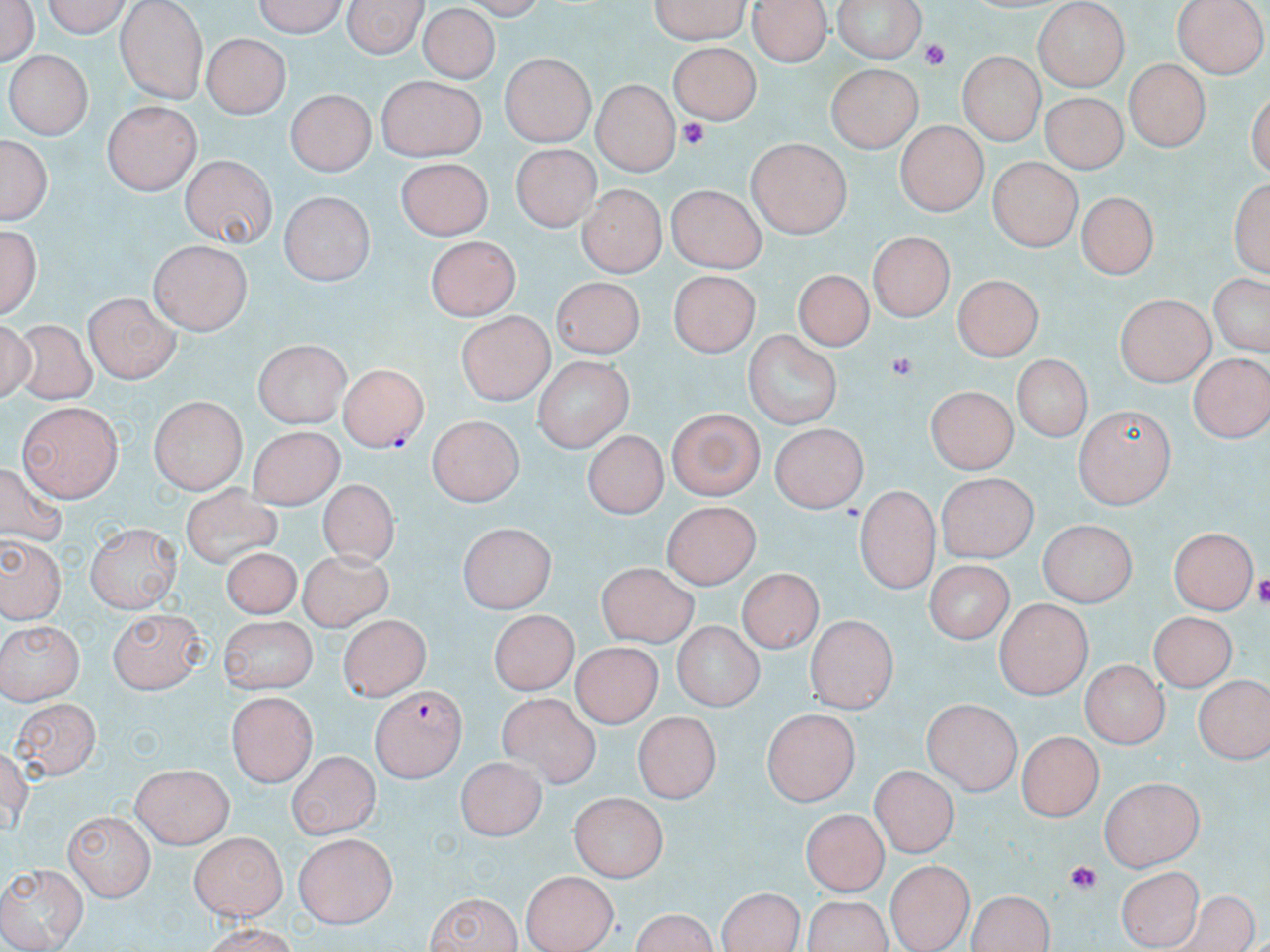

slide_level_diagnosis: Plasmodium falciparum
magnification: 1000x
image_size: 1270×952 pixels
modality: light microscopy
stain: May-Grünwald-Giemsa
field_of_view: one of a larger specimen
preparation: thin blood smear
platelet_locations: 'approximate bounding boxes as named x1/y1/x2/y2 corners in pixels: (x1=921, y1=40, x2=955, y2=70), (x1=676, y1=118, x2=709, y2=149), (x1=889, y1=353, x2=913, y2=379), (x1=1257, y1=575, x2=1270, y2=607), (x1=1065, y1=858, x2=1099, y2=896)'
plasmodium_falciparum_infected_red_blood_cell_locations: 'approximate bounding boxes as named x1/y1/x2/y2 corners in pixels: (x1=335, y1=364, x2=428, y2=452), (x1=370, y1=686, x2=465, y2=782)'
uninfected_red_blood_cell_locations: 'approximate bounding boxes as named x1/y1/x2/y2 corners in pixels: (x1=0, y1=0, x2=39, y2=70), (x1=35, y1=0, x2=134, y2=35), (x1=247, y1=0, x2=349, y2=35), (x1=345, y1=0, x2=421, y2=60), (x1=647, y1=0, x2=752, y2=39), (x1=831, y1=0, x2=928, y2=61), (x1=1173, y1=0, x2=1266, y2=77), (x1=114, y1=1, x2=210, y2=103), (x1=749, y1=1, x2=833, y2=63), (x1=1032, y1=3, x2=1132, y2=89), (x1=421, y1=7, x2=497, y2=80), (x1=401, y1=21, x2=497, y2=133), (x1=203, y1=32, x2=287, y2=119), (x1=668, y1=40, x2=762, y2=127), (x1=959, y1=51, x2=1043, y2=143), (x1=10, y1=52, x2=92, y2=138), (x1=501, y1=55, x2=594, y2=147), (x1=1124, y1=59, x2=1208, y2=153), (x1=829, y1=66, x2=921, y2=152), (x1=374, y1=73, x2=488, y2=161), (x1=593, y1=79, x2=680, y2=173), (x1=286, y1=89, x2=373, y2=177), (x1=1041, y1=95, x2=1122, y2=174), (x1=101, y1=99, x2=199, y2=192), (x1=897, y1=121, x2=984, y2=218), (x1=0, y1=135, x2=54, y2=224), (x1=744, y1=137, x2=852, y2=239), (x1=510, y1=144, x2=600, y2=232), (x1=180, y1=155, x2=276, y2=249), (x1=989, y1=155, x2=1085, y2=248), (x1=394, y1=158, x2=492, y2=236), (x1=1231, y1=178, x2=1269, y2=276), (x1=667, y1=183, x2=766, y2=274), (x1=577, y1=185, x2=662, y2=277), (x1=1077, y1=191, x2=1157, y2=282), (x1=276, y1=192, x2=376, y2=285), (x1=1, y1=226, x2=43, y2=323), (x1=870, y1=231, x2=957, y2=318), (x1=427, y1=234, x2=523, y2=317), (x1=149, y1=240, x2=253, y2=335), (x1=669, y1=269, x2=761, y2=357), (x1=793, y1=269, x2=870, y2=353), (x1=1205, y1=271, x2=1268, y2=357), (x1=955, y1=273, x2=1045, y2=358), (x1=551, y1=277, x2=643, y2=355), (x1=81, y1=293, x2=182, y2=382), (x1=1115, y1=293, x2=1213, y2=385), (x1=456, y1=313, x2=553, y2=406), (x1=8, y1=324, x2=100, y2=403), (x1=741, y1=329, x2=845, y2=430), (x1=256, y1=341, x2=350, y2=428), (x1=1189, y1=351, x2=1270, y2=439), (x1=1009, y1=355, x2=1095, y2=441), (x1=533, y1=356, x2=632, y2=453), (x1=926, y1=388, x2=1021, y2=472), (x1=149, y1=396, x2=245, y2=492), (x1=17, y1=401, x2=119, y2=501), (x1=665, y1=407, x2=764, y2=499), (x1=1076, y1=407, x2=1175, y2=510), (x1=425, y1=416, x2=526, y2=504), (x1=768, y1=420, x2=867, y2=513), (x1=246, y1=425, x2=340, y2=510), (x1=581, y1=432, x2=668, y2=517), (x1=935, y1=474, x2=1034, y2=562), (x1=316, y1=481, x2=401, y2=565), (x1=177, y1=483, x2=284, y2=571), (x1=854, y1=487, x2=942, y2=591), (x1=664, y1=501, x2=761, y2=589), (x1=1037, y1=521, x2=1134, y2=607), (x1=86, y1=524, x2=181, y2=614), (x1=456, y1=524, x2=558, y2=613), (x1=1171, y1=525, x2=1258, y2=615), (x1=3, y1=537, x2=60, y2=622), (x1=221, y1=545, x2=299, y2=621), (x1=296, y1=552, x2=396, y2=631), (x1=928, y1=561, x2=1011, y2=641), (x1=598, y1=563, x2=698, y2=647), (x1=740, y1=567, x2=820, y2=654), (x1=994, y1=599, x2=1092, y2=696), (x1=105, y1=606, x2=206, y2=693), (x1=485, y1=608, x2=582, y2=692), (x1=1150, y1=609, x2=1239, y2=693), (x1=805, y1=614, x2=898, y2=714), (x1=336, y1=615, x2=429, y2=699), (x1=217, y1=617, x2=320, y2=695), (x1=0, y1=619, x2=84, y2=703), (x1=669, y1=625, x2=763, y2=709), (x1=571, y1=644, x2=661, y2=730), (x1=1083, y1=660, x2=1168, y2=747), (x1=1193, y1=675, x2=1267, y2=761), (x1=227, y1=690, x2=314, y2=787), (x1=497, y1=692, x2=600, y2=789), (x1=12, y1=697, x2=96, y2=778), (x1=920, y1=699, x2=1024, y2=793), (x1=762, y1=706, x2=864, y2=805), (x1=634, y1=711, x2=718, y2=805), (x1=1019, y1=729, x2=1101, y2=821), (x1=1, y1=745, x2=38, y2=837), (x1=289, y1=750, x2=379, y2=838), (x1=454, y1=756, x2=542, y2=840), (x1=131, y1=763, x2=231, y2=847), (x1=868, y1=766, x2=956, y2=856), (x1=1099, y1=776, x2=1206, y2=871), (x1=78, y1=787, x2=223, y2=865), (x1=573, y1=795, x2=667, y2=882), (x1=803, y1=806, x2=889, y2=893), (x1=67, y1=810, x2=153, y2=898), (x1=188, y1=831, x2=289, y2=923), (x1=294, y1=831, x2=398, y2=926), (x1=0, y1=860, x2=89, y2=950), (x1=883, y1=860, x2=970, y2=950), (x1=1118, y1=863, x2=1205, y2=950), (x1=521, y1=871, x2=618, y2=952), (x1=715, y1=885, x2=809, y2=952), (x1=806, y1=890, x2=892, y2=951), (x1=965, y1=890, x2=1057, y2=952), (x1=424, y1=892, x2=523, y2=951), (x1=1173, y1=896, x2=1262, y2=952), (x1=627, y1=909, x2=722, y2=952), (x1=198, y1=923, x2=301, y2=952)'